Classify this cell by malaria status.
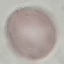

Uninfected.

Summary:
  - Image type: automatically extracted cell patch, resized to 64 × 64 pixels
  - Stain: Giemsa
  - Capture: smartphone camera at the microscope eyepiece
  - Preparation: thin blood smear